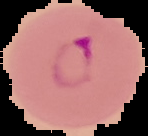
{
  "image_size": "148×136 pixels",
  "malaria_status": "parasitized",
  "image_type": "cell region segmented out of the field of view; surrounding area masked to black",
  "preparation": "thin blood smear"
}